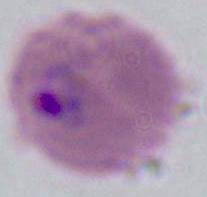
Summary:
  - Magnification: 400x or 1000x
  - Identification: Plasmodium
  - Modality: micrograph